Locate and identify every blood parasite.
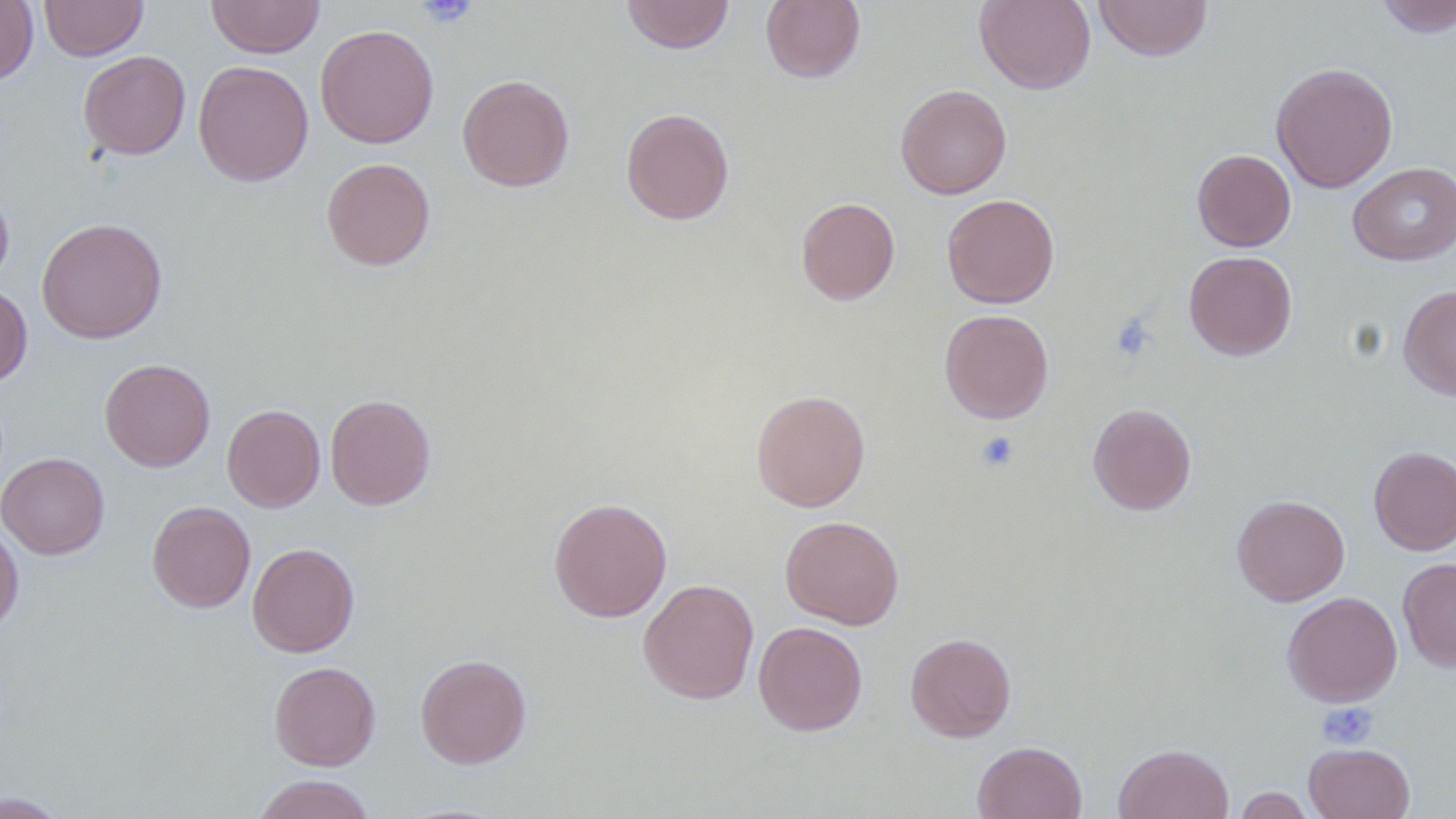

No blood parasites seen.

Approximate bounding boxes as (x1, y1, x2, y2) in pixels. Platelet locations: (417, 0, 480, 28), (1111, 312, 1157, 362), (976, 432, 1020, 473), (1317, 702, 1377, 749). Uninfected red blood cell locations: (40, 0, 148, 60), (206, 0, 324, 58), (621, 0, 735, 54), (760, 0, 865, 84), (974, 0, 1096, 94), (1093, 0, 1213, 62), (1374, 0, 1456, 37), (0, 1, 38, 85), (315, 24, 439, 148), (78, 50, 190, 159), (193, 60, 313, 186), (1270, 61, 1398, 193), (458, 74, 575, 191), (895, 84, 1012, 199), (621, 107, 735, 224), (1192, 149, 1296, 251), (321, 157, 435, 270), (1347, 161, 1456, 266), (0, 180, 14, 290), (941, 193, 1059, 308), (796, 197, 900, 305), (36, 218, 167, 343), (1184, 251, 1297, 360), (0, 284, 32, 386), (1398, 284, 1456, 400), (939, 308, 1054, 424), (100, 358, 215, 472), (751, 389, 870, 512), (325, 393, 435, 510), (1087, 403, 1196, 515), (222, 404, 325, 511), (1369, 446, 1456, 555), (0, 452, 109, 559), (1232, 494, 1350, 605), (548, 497, 672, 622), (146, 500, 255, 612), (780, 515, 904, 629), (0, 522, 24, 635), (247, 542, 359, 657), (1398, 558, 1456, 671), (639, 578, 759, 704), (1282, 591, 1402, 706), (753, 621, 868, 736), (905, 632, 1016, 742), (415, 653, 531, 768), (269, 661, 381, 770), (972, 741, 1086, 819), (1304, 742, 1415, 819), (1113, 743, 1233, 819), (253, 774, 375, 819), (1232, 786, 1316, 818), (0, 791, 70, 818). Slide-level diagnosis: negative for blood parasites. 1000x magnification. Image is 1456×819 pixels. Single field of view. Thin blood film. Light microscopy.